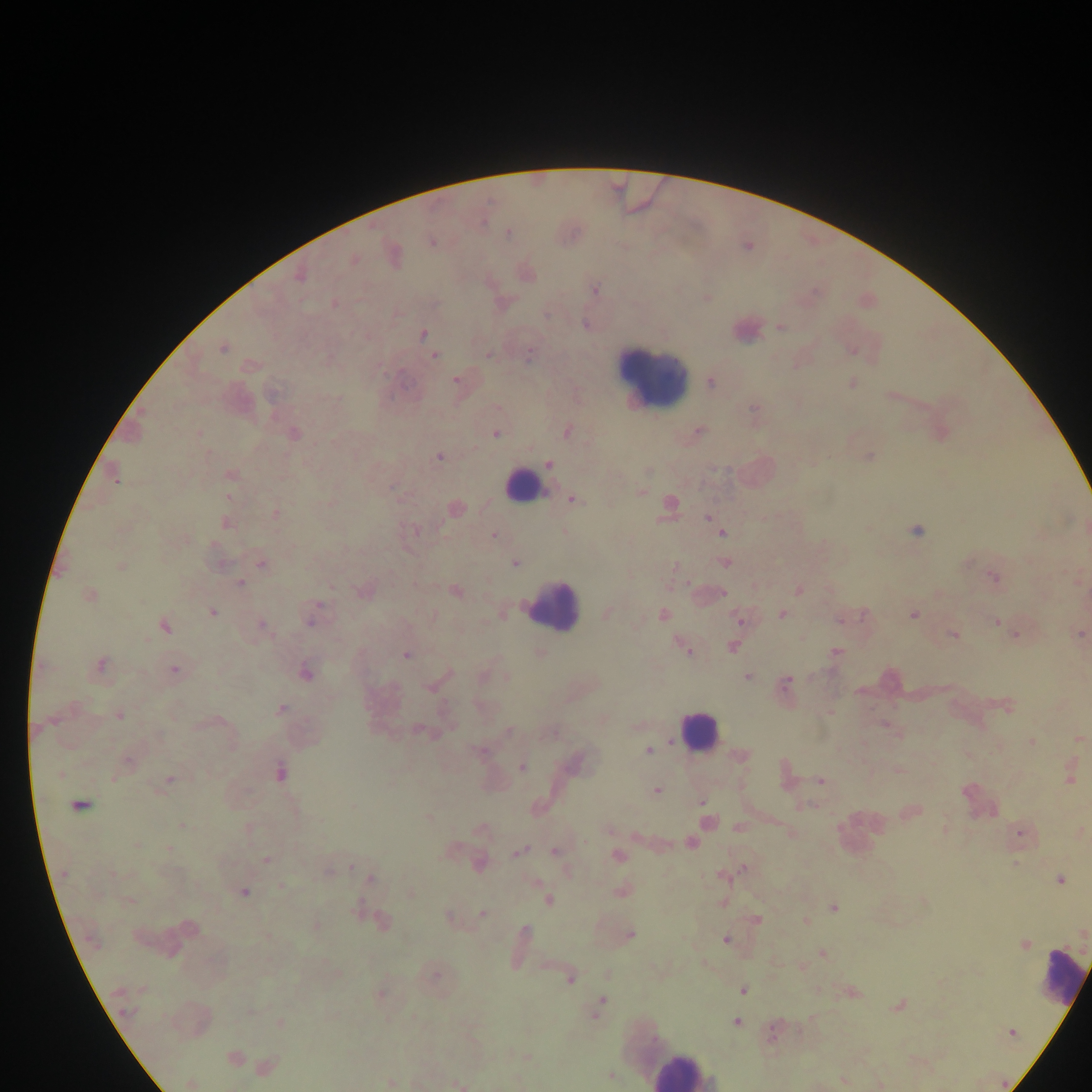
capture = mobile-phone photograph through a microscope
field of view = single
preparation = thick blood smear
country = Ghana
malaria parasite locations = approximate centers as [x, y] in pixels: [509, 233], [432, 243], [354, 260], [299, 276], [595, 290], [334, 303], [780, 326], [422, 335], [222, 348], [434, 355], [487, 355], [528, 356], [456, 380], [711, 383], [852, 383], [754, 410], [699, 431], [567, 432], [199, 433], [495, 433], [294, 434], [869, 456], [439, 457], [549, 464], [231, 475], [115, 478], [642, 492], [228, 497], [573, 500], [669, 506], [455, 508], [275, 513], [707, 517], [226, 524], [415, 531], [565, 532], [916, 532], [722, 533], [493, 536], [726, 563], [261, 564], [516, 564], [121, 567], [993, 578], [240, 582], [798, 590], [455, 591], [723, 594], [89, 595], [212, 612], [607, 613], [781, 614], [663, 615], [913, 615], [311, 620], [740, 620], [996, 622], [263, 625], [165, 627], [1014, 634], [953, 635], [1080, 635], [732, 647], [684, 648], [835, 652], [540, 654], [406, 656], [101, 665], [174, 670], [306, 673], [506, 676], [747, 677], [787, 683], [429, 688], [1007, 706], [281, 710], [119, 715], [885, 725], [419, 731], [508, 731], [1080, 739], [1032, 742], [481, 751], [648, 751], [742, 755], [128, 762], [523, 767], [899, 770], [280, 773], [60, 775], [785, 775], [114, 778], [170, 779], [1070, 779], [821, 781], [656, 791], [702, 802], [79, 805], [354, 806], [914, 811], [705, 813], [429, 818], [707, 823], [182, 825], [740, 827], [482, 828], [609, 829], [945, 829], [791, 833], [1020, 835], [691, 844], [137, 845], [169, 849], [518, 851], [556, 852], [618, 856], [267, 860], [1015, 863], [480, 864], [350, 867], [743, 869], [329, 870], [64, 873], [112, 873], [725, 875], [371, 880], [1060, 880], [535, 882], [281, 887], [622, 891], [243, 892], [130, 901], [549, 901], [834, 908], [482, 914], [449, 917], [756, 920], [382, 921], [806, 922], [317, 925], [525, 932], [1083, 933], [630, 934], [267, 936], [726, 940], [1025, 945], [822, 953], [435, 975], [570, 979], [743, 991], [853, 993], [380, 994], [601, 1004], [898, 1005], [597, 1012], [127, 1013], [736, 1022], [280, 1023], [1012, 1032], [772, 1035], [234, 1057], [526, 1057], [265, 1067], [610, 1076], [842, 1080], [391, 1082], [190, 1083], [459, 1085]
leukocyte locations = approximate centers as [x, y] in pixels: [650, 374], [521, 484], [553, 604], [699, 732], [1060, 977], [682, 1070]
image size = 1092×1092 pixels